State the blood parasite species.
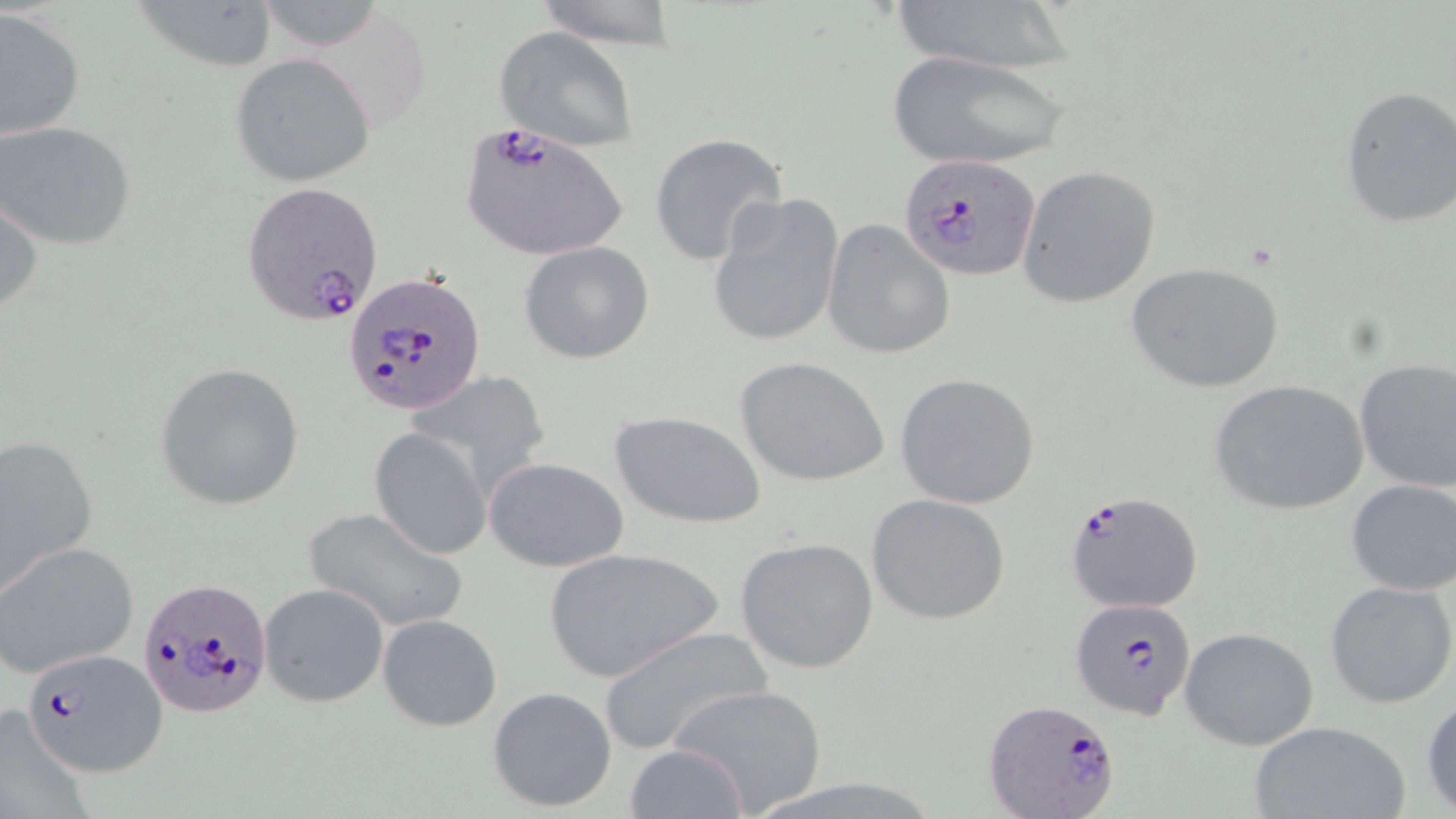

Plasmodium falciparum.

Approximate bounding boxes as (x1, y1, x2, y2) in pixels. Plasmodium falciparum-infected red blood cell locations: (459, 120, 628, 262), (900, 153, 1040, 282), (241, 181, 386, 327), (344, 272, 486, 414), (1063, 487, 1207, 613), (141, 578, 272, 717), (1071, 598, 1198, 720), (23, 647, 164, 779), (982, 697, 1122, 819). Uninfected red blood cell locations: (134, 0, 280, 74), (531, 0, 682, 50), (884, 0, 1084, 75), (0, 8, 84, 138), (495, 26, 639, 152), (885, 50, 1070, 170), (230, 53, 376, 187), (1339, 85, 1456, 228), (0, 120, 137, 250), (650, 132, 788, 267), (1016, 165, 1162, 309), (1, 190, 42, 321), (705, 192, 845, 349), (821, 218, 954, 360), (518, 240, 655, 364), (1127, 261, 1286, 396), (734, 355, 890, 487), (1354, 359, 1456, 493), (155, 362, 305, 511), (410, 371, 554, 499), (894, 372, 1042, 510), (1207, 378, 1369, 517), (607, 409, 767, 529), (369, 428, 490, 559), (0, 434, 100, 594), (483, 456, 629, 573), (1345, 478, 1456, 596), (865, 492, 1012, 627), (303, 507, 469, 634), (734, 537, 880, 674), (0, 540, 141, 679), (543, 546, 722, 682), (1325, 580, 1456, 707), (259, 582, 389, 708), (377, 612, 503, 732), (600, 625, 772, 757), (1179, 626, 1319, 750), (670, 682, 828, 815), (487, 686, 618, 813), (1422, 690, 1455, 815), (0, 703, 94, 819), (1246, 720, 1412, 819), (625, 743, 747, 819). Single field of view. Thin blood smear. Image is 1456×819 pixels. Captured at 1000x magnification. Light microscopy. May-Grünwald-Giemsa-stained preparation.